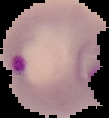
preparation = thin blood smear
image type = segmented cell region with the area outside set to black
malaria status = parasitized
image size = 109×118 pixels